Identify the parasite.
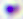

This is Toxoplasma gondii.

magnification = 400x
modality = photomicrograph